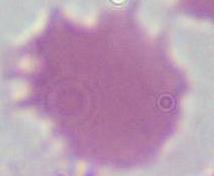

{
  "identification": "red blood cell",
  "modality": "photomicrograph",
  "magnification": "1000x"
}